Name the parasite shown.
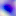

This is Toxoplasma gondii.

Summary:
  - Modality: photomicrograph
  - Magnification: 400x